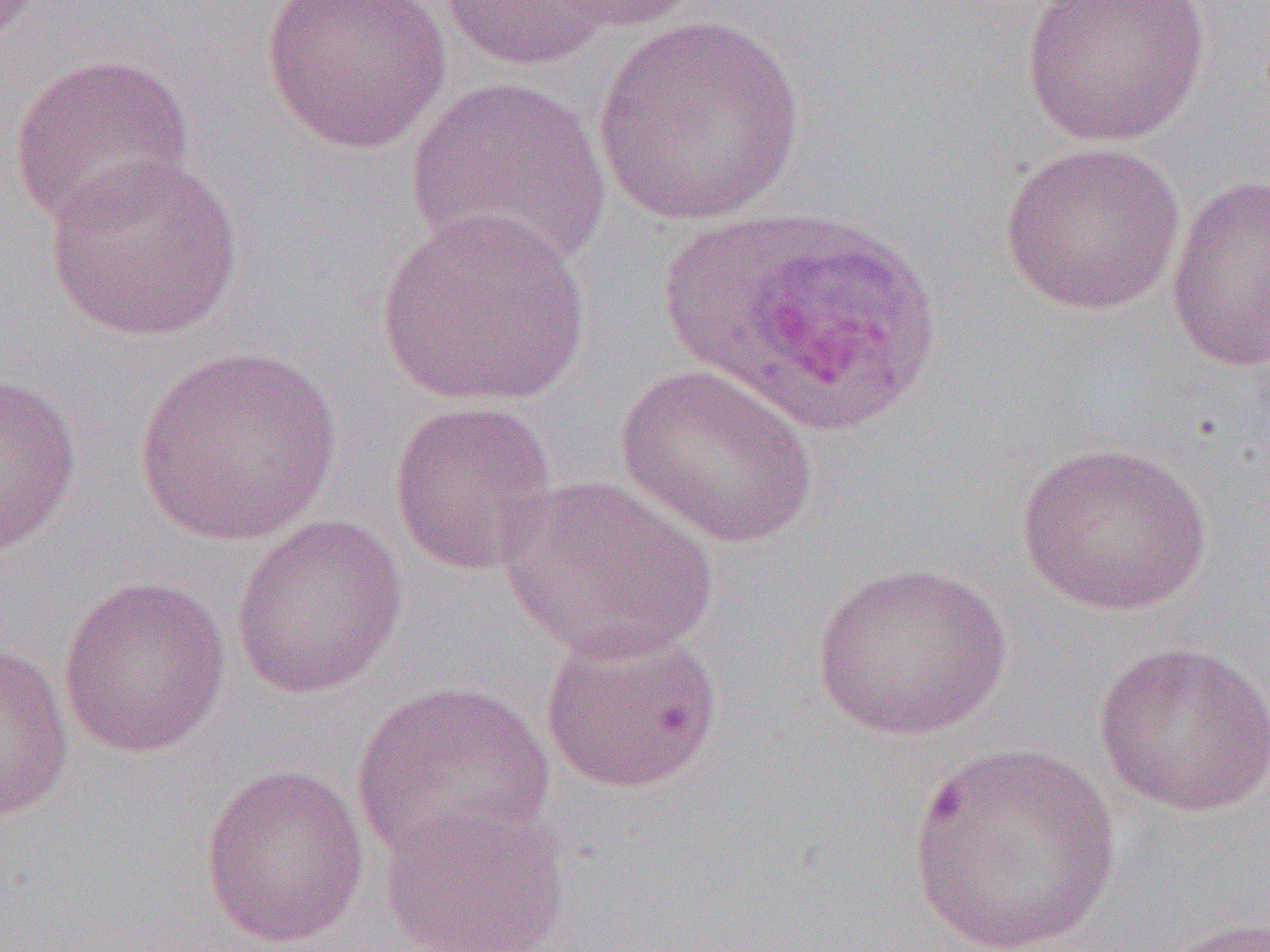
{
  "slide_level_diagnosis": "Plasmodium ovale",
  "image_size": "1270×952 pixels",
  "preparation": "thin blood smear",
  "modality": "optical microscopy",
  "uninfected_red_blood_cell_locations_subset": "approximate bounding boxes as named x1/y1/x2/y2 corners in pixels: (x1=260, y1=0, x2=452, y2=154), (x1=541, y1=0, x2=704, y2=34), (x1=1021, y1=0, x2=1210, y2=148), (x1=437, y1=1, x2=611, y2=72), (x1=592, y1=15, x2=807, y2=227), (x1=8, y1=53, x2=196, y2=231), (x1=407, y1=75, x2=612, y2=274), (x1=997, y1=140, x2=1187, y2=316), (x1=43, y1=153, x2=245, y2=341), (x1=1165, y1=174, x2=1270, y2=372), (x1=375, y1=209, x2=592, y2=410), (x1=132, y1=346, x2=344, y2=547), (x1=615, y1=363, x2=819, y2=549), (x1=0, y1=373, x2=83, y2=556), (x1=388, y1=399, x2=559, y2=576), (x1=1016, y1=442, x2=1214, y2=616), (x1=499, y1=473, x2=718, y2=663), (x1=230, y1=515, x2=408, y2=700), (x1=810, y1=561, x2=1013, y2=741), (x1=57, y1=575, x2=231, y2=760), (x1=539, y1=621, x2=725, y2=796), (x1=1094, y1=640, x2=1270, y2=816), (x1=0, y1=642, x2=74, y2=823), (x1=351, y1=679, x2=555, y2=867), (x1=907, y1=742, x2=1122, y2=951), (x1=199, y1=762, x2=371, y2=949), (x1=377, y1=800, x2=570, y2=952), (x1=1160, y1=916, x2=1270, y2=952)",
  "field_of_view": "one of a larger specimen",
  "magnification": "1000x"
}